Find the cells and give the type of each one.
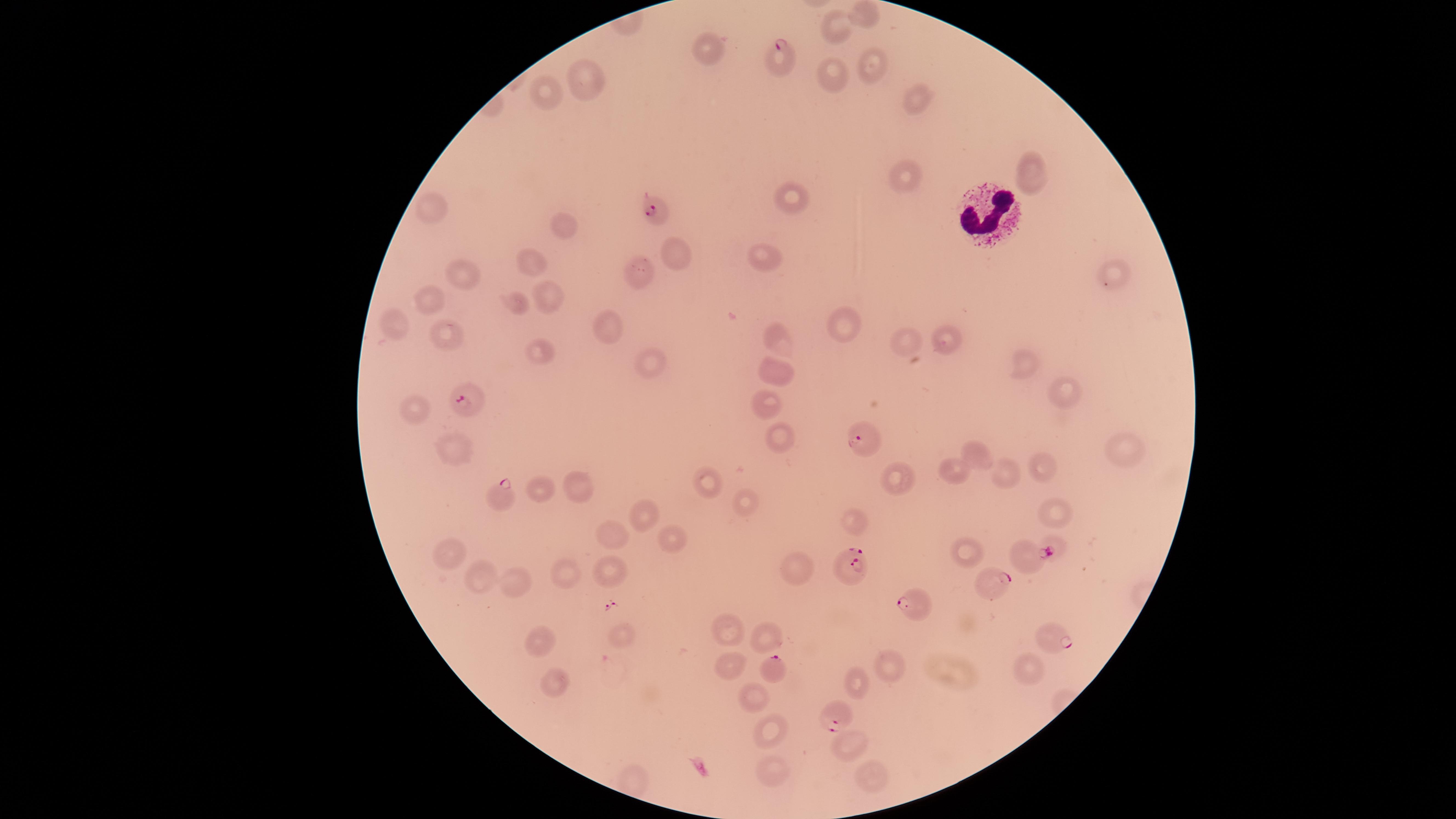

Approximate marker points as (x, y) in pixels.
Parasitized RBCs: (783, 56), (656, 212), (465, 403), (861, 437), (501, 495), (1027, 556), (848, 570), (999, 583), (913, 601), (1052, 637), (772, 668), (836, 713).
Uninfected RBCs: (862, 14), (836, 24), (709, 48), (868, 66), (831, 75), (588, 80), (552, 94), (915, 97), (1030, 173), (906, 179), (790, 199), (432, 209), (564, 227), (670, 256), (771, 258), (536, 262), (462, 273), (638, 273), (1108, 275), (521, 298), (551, 300), (434, 303), (391, 326), (841, 328), (608, 330), (780, 338), (445, 339), (910, 341), (946, 342), (540, 350), (646, 362), (1026, 363), (777, 371), (1064, 392), (766, 397), (415, 410), (776, 434), (1124, 451), (979, 453), (448, 456), (1040, 464), (959, 467), (895, 475), (1001, 476), (708, 481), (577, 486), (537, 489), (743, 507), (1053, 513), (642, 514), (857, 525), (609, 537), (671, 537), (1053, 544), (966, 551), (454, 555), (564, 575), (611, 577), (801, 577), (478, 578), (508, 584), (727, 628), (769, 636), (620, 637), (535, 640), (730, 664), (1029, 666), (887, 668), (555, 670), (857, 683), (750, 695), (767, 736), (850, 744), (771, 773), (867, 780).
WBCs: (987, 213).

stain: Giemsa
image_size: 1456×819 pixels
capture: smartphone photograph through the microscope eyepiece
visible_region: circular
preparation: thin blood smear
field_of_view: single
species: Plasmodium falciparum